Locate every blood parasite and identify its species.
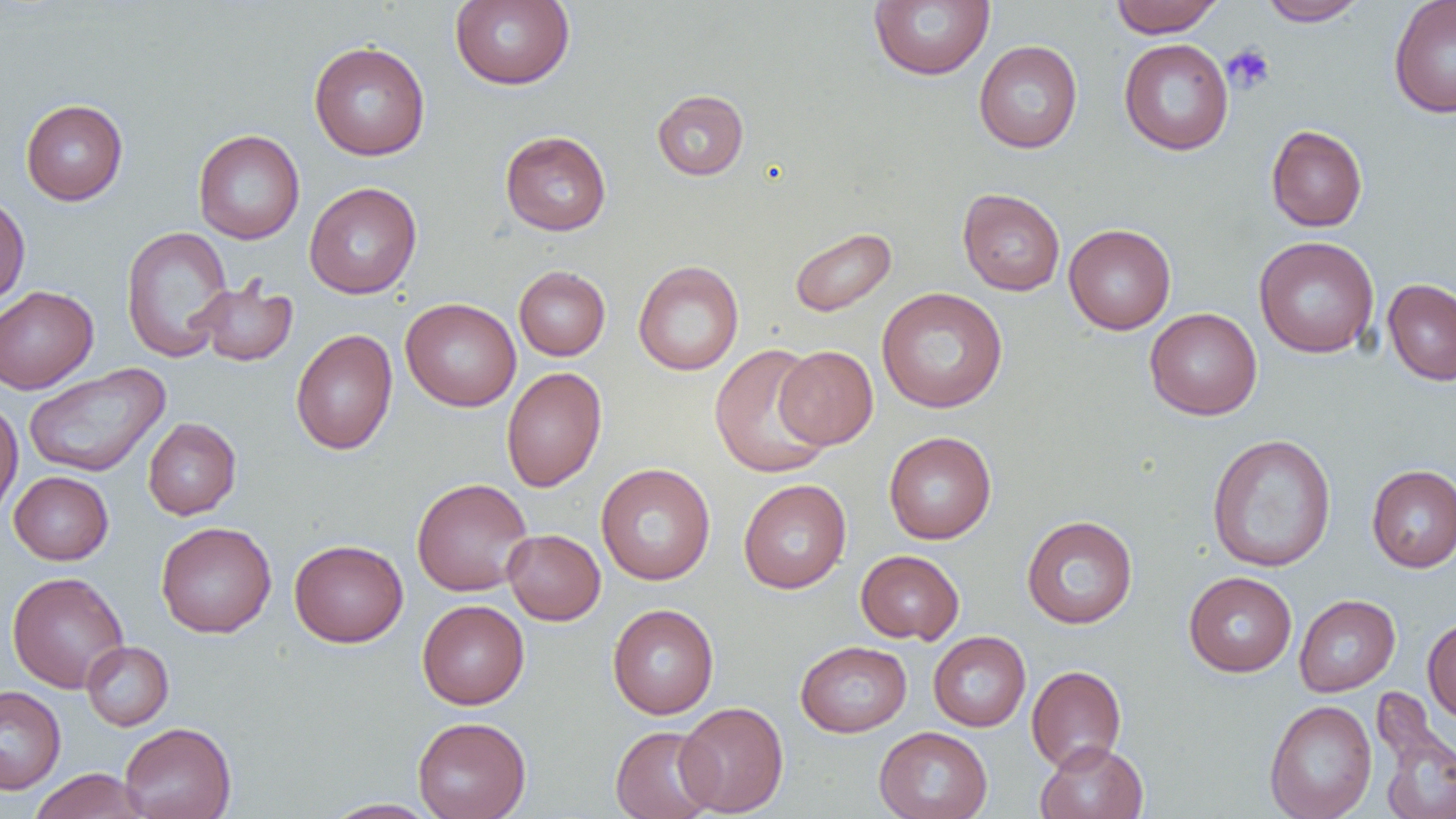

No blood parasites observed.

Approximate bounding boxes as [x1, y1, x2, y2] in pixels. Platelet locations: [1222, 43, 1275, 94]. Uninfected red blood cell locations: [450, 0, 575, 89], [868, 0, 995, 81], [1110, 0, 1223, 37], [1258, 0, 1368, 26], [1388, 0, 1456, 118], [1119, 39, 1234, 155], [973, 40, 1083, 153], [308, 41, 431, 160], [652, 89, 749, 180], [20, 99, 128, 205], [1266, 124, 1368, 231], [193, 129, 305, 244], [500, 130, 611, 235], [304, 181, 422, 299], [957, 188, 1066, 296], [0, 193, 30, 307], [1063, 223, 1176, 334], [120, 226, 234, 362], [788, 227, 896, 317], [1254, 236, 1379, 358], [633, 260, 744, 375], [514, 266, 610, 361], [190, 277, 299, 366], [1383, 278, 1456, 386], [0, 286, 98, 394], [877, 287, 1008, 413], [400, 298, 521, 411], [1144, 307, 1262, 420], [291, 329, 398, 455], [709, 343, 834, 478], [775, 345, 878, 449], [23, 364, 170, 478], [501, 367, 607, 492], [0, 400, 23, 523], [143, 417, 241, 519], [883, 431, 996, 544], [1206, 433, 1337, 572], [596, 463, 715, 585], [1366, 464, 1456, 572], [8, 471, 113, 565], [412, 478, 533, 596], [738, 479, 851, 593], [1021, 515, 1138, 629], [156, 521, 276, 638], [502, 529, 605, 625], [289, 539, 408, 647], [855, 550, 964, 644], [7, 571, 129, 693], [1184, 571, 1297, 677], [1293, 594, 1400, 696], [417, 600, 529, 709], [607, 603, 719, 719], [1422, 616, 1456, 723], [928, 631, 1030, 731], [795, 640, 912, 737], [81, 641, 173, 730], [1026, 665, 1126, 772], [0, 686, 66, 794], [1372, 689, 1456, 819], [1264, 699, 1377, 819], [676, 701, 789, 816], [413, 716, 531, 819], [119, 722, 236, 819], [610, 725, 719, 819], [874, 726, 993, 819], [1035, 740, 1148, 819], [28, 768, 149, 819], [321, 798, 442, 818]. Slide-level diagnosis: no evidence of blood parasites. One field of a larger specimen. Light microscopy. Image is 1456×819 pixels. 1000x magnification. Thin blood smear.